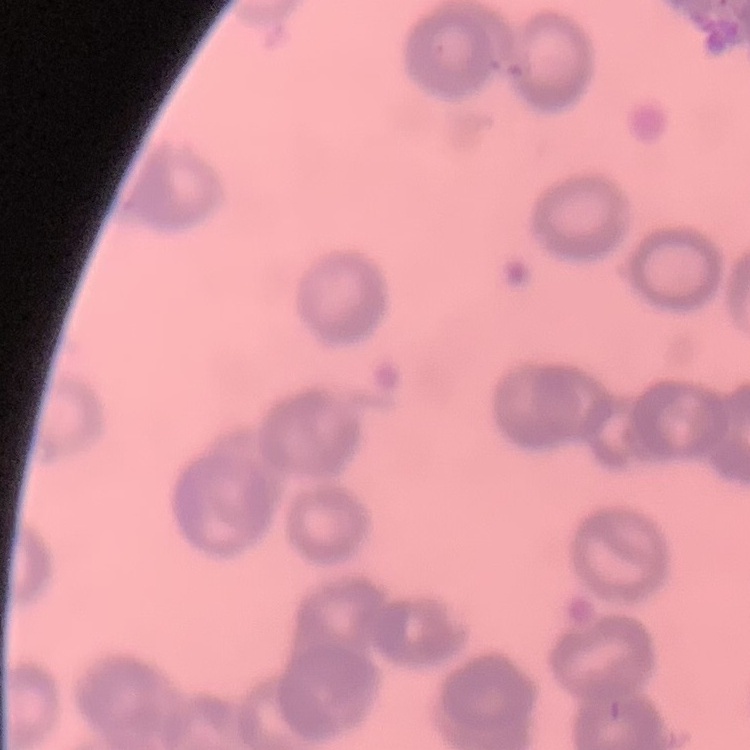
The erythrocytes show rouleaux formation. Stained with either Field's or Giemsa. One tile cut from a larger photomicrograph. Thin blood film.